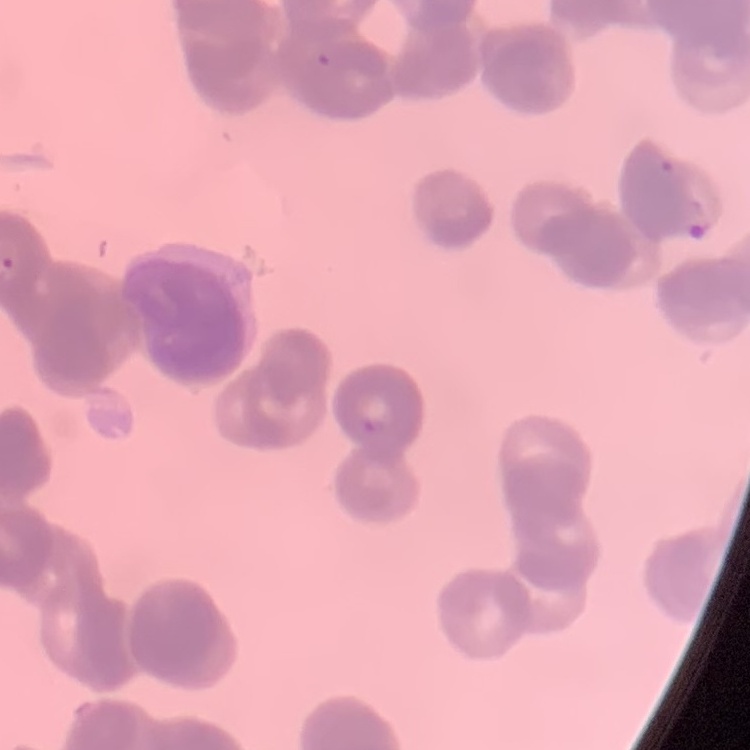

Summary:
  - Erythrocyte morphology: rouleaux formation
  - Image type: one tile cut from a larger photomicrograph
  - Stain: Field's or Giemsa
  - Preparation: thin blood film